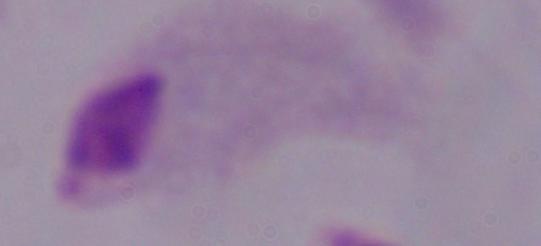 A trichomonad is seen. Photomicrograph. Captured at 1000x magnification.